Locate every malaria parasite.
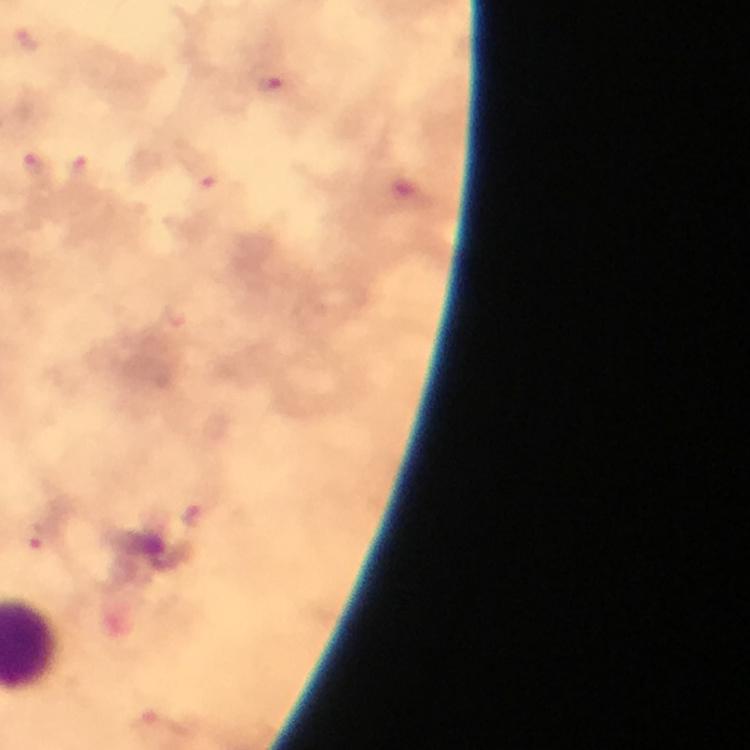

Approximate centers as [x, y] in pixels.
Malaria parasites: [26, 38], [31, 165], [78, 166], [206, 180], [43, 537].

Summary:
  - Cropped from: a single field of view
  - Stain: Giemsa
  - Magnification: 100x
  - Immersion oil: applied
  - Context: from a malaria diagnostic workup
  - Preparation: thick blood smear
  - Image size: 750×750 pixels
  - Capture: smartphone photograph through a microscope